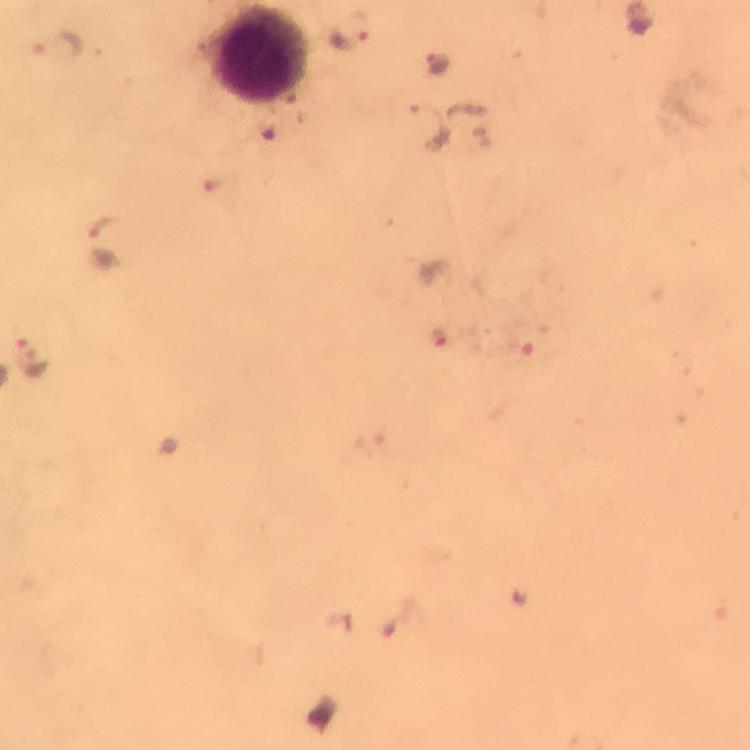 Approximate centers as {x, y} in pixels. Plasmodium parasite locations: {350, 29}, {60, 44}, {440, 64}, {430, 124}, {104, 226}, {439, 337}, {32, 355}. Leukocyte locations: {258, 54}. Cropped region of a single field of view. From a diagnostic examination for malaria. Image is 750×750 pixels. Giemsa stain. Immersion oil was used. Photographed with a smartphone mounted on the microscope. At 100x magnification. Thick blood smear.